State which parasite is depicted.
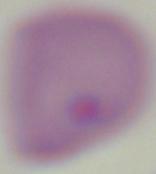
Babesia.

modality: micrograph
magnification: 1000x